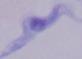

1000x magnification. A trypanosome is shown. Photomicrograph.